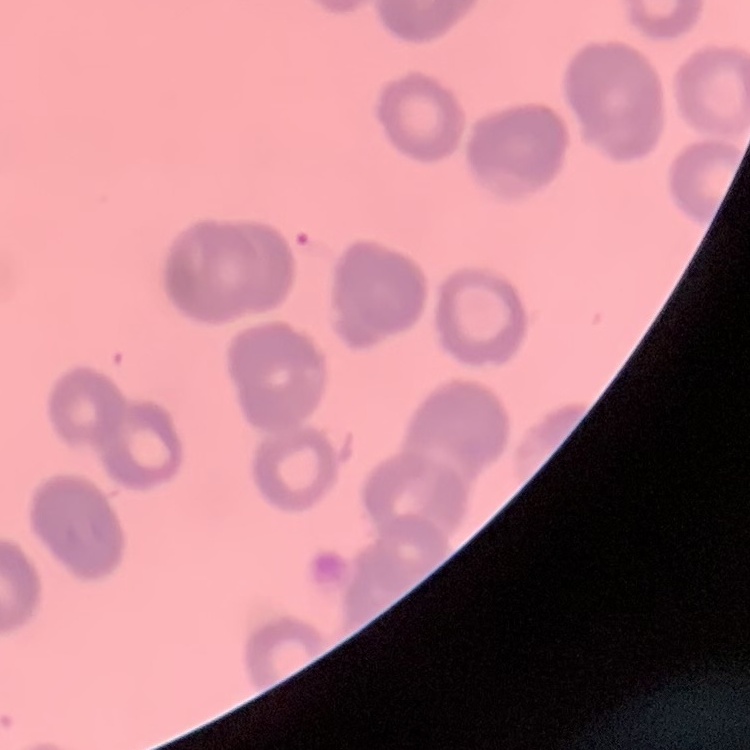

The red blood cells show rouleaux formation. One tile cut from a larger photomicrograph. Thin peripheral smear. Stained with either Field's or Giemsa.